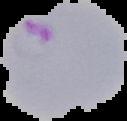

From a thin blood smear. Result: malaria parasites identified. Image is 127×121 pixels. Segmented cell region on a black background.